Identify the parasite.
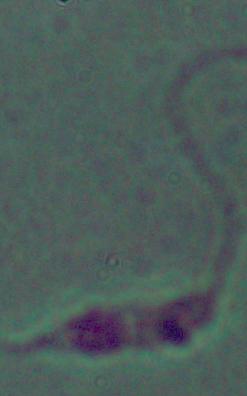
Leishmania.

Photomicrograph. Captured at 1000x magnification.